Assess this cell for malaria.
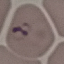
Parasitized.

Photographed with a smartphone camera at the microscope eyepiece. Giemsa stain. Thin smear of blood. Automatically extracted cell patch, resized to 64 × 64 pixels.